Find each parasitized RBC.
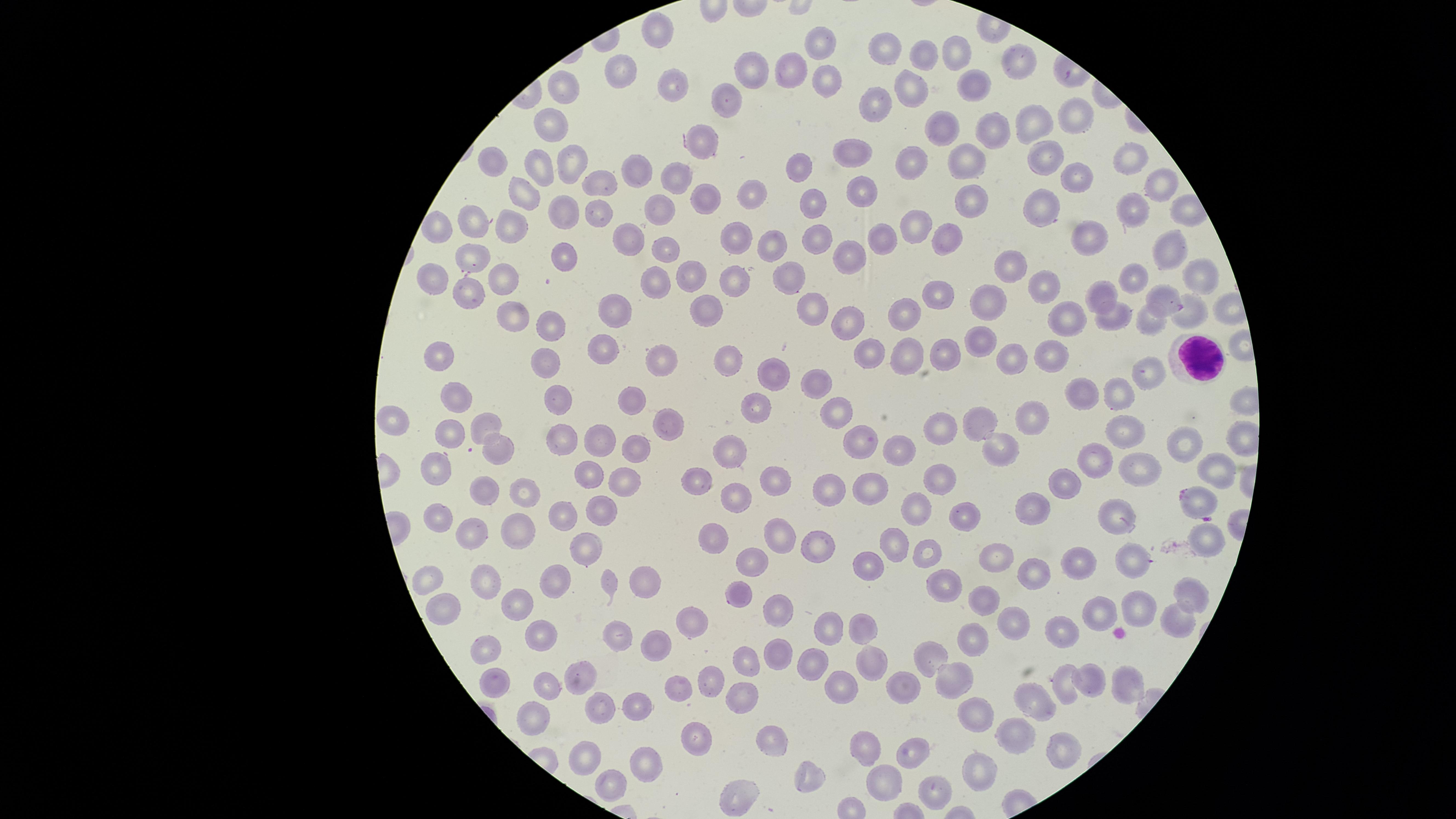
Approximate marker points as [x, y] in pixels.
Parasitized RBCs: [1166, 300], [1197, 503].

Approximate marker points as [x, y] in pixels.
Summary:
  - Uninfected RBCs: [658, 31], [822, 40], [890, 43], [926, 53], [958, 59], [1021, 65], [764, 71], [621, 73], [793, 74], [909, 81], [829, 82], [674, 85], [560, 86], [978, 86], [733, 93], [874, 104], [1079, 117], [551, 124], [1035, 126], [994, 129], [939, 130], [702, 141], [852, 155], [1043, 156], [1130, 157], [975, 158], [913, 161], [494, 163], [569, 165], [542, 168], [799, 170], [636, 174], [1075, 175], [673, 179], [1158, 181], [606, 185], [863, 191], [525, 194], [749, 194], [702, 197], [1041, 197], [811, 200], [968, 200], [1133, 207], [662, 209], [561, 210], [597, 217], [916, 224], [516, 225], [475, 226], [739, 233], [1096, 235], [629, 236], [819, 238], [881, 239], [943, 241], [1172, 242], [772, 246], [663, 250], [567, 255], [847, 255], [478, 260], [1017, 264], [686, 274], [1200, 276], [1134, 277], [785, 278], [432, 280], [737, 282], [653, 283], [503, 286], [1043, 289], [467, 291], [1099, 292], [938, 293], [984, 298], [711, 305], [617, 307], [1189, 309], [810, 312], [903, 312], [514, 313], [1069, 321], [1111, 322], [1147, 322], [551, 328], [847, 328], [607, 340], [980, 340], [871, 350], [944, 352], [1049, 353], [446, 355], [904, 355], [1016, 358], [724, 359], [546, 360], [662, 364], [1151, 369], [776, 374], [817, 387], [459, 391], [1116, 391], [1078, 396], [634, 400], [558, 401], [753, 407], [1039, 411], [833, 414], [974, 417], [934, 420], [398, 422], [492, 423], [1120, 424], [670, 427], [452, 436], [563, 436], [862, 436], [599, 439], [500, 446], [637, 446], [1191, 446], [999, 447], [897, 449], [739, 454], [1096, 457], [587, 468], [1137, 468], [1209, 468], [438, 469], [699, 478], [941, 481], [622, 484], [1064, 485], [831, 487], [778, 488], [871, 488], [487, 489], [526, 495], [740, 495], [923, 506], [604, 507], [1108, 509], [1029, 510], [561, 512], [964, 513], [440, 520], [470, 528], [515, 530], [1203, 535], [716, 536], [777, 540], [892, 541], [584, 543], [818, 543], [928, 547], [1130, 558], [861, 561], [751, 564], [1002, 564], [1083, 567], [1029, 573], [561, 574], [433, 580], [487, 580], [648, 580], [943, 584], [609, 585], [739, 594], [1191, 597], [518, 598], [986, 601], [445, 606], [1135, 608], [779, 612], [1098, 614], [861, 618], [1017, 618], [690, 619], [1177, 621], [542, 625], [828, 627], [1060, 634], [614, 635], [975, 635], [492, 648], [650, 648], [778, 649], [872, 659], [813, 660], [927, 660], [746, 663], [582, 674], [1089, 674], [496, 679], [945, 679], [712, 681], [1124, 681], [836, 682], [1066, 684], [553, 685], [901, 686], [737, 695], [1037, 700], [606, 708], [641, 711], [532, 719], [973, 722], [1020, 733], [775, 737], [694, 744], [1058, 748], [861, 749], [583, 753], [909, 755], [644, 760], [985, 766], [806, 771], [617, 778], [890, 780], [742, 793], [938, 794]
  - WBCs: [1190, 359]
  - Preparation: thin smear of blood
  - Stain: Giemsa
  - Visible region: circular
  - Capture: smartphone photograph through the microscope eyepiece
  - Image size: 1456×819 pixels
  - Field of view: single
  - Species: Plasmodium falciparum